State which parasite is depicted.
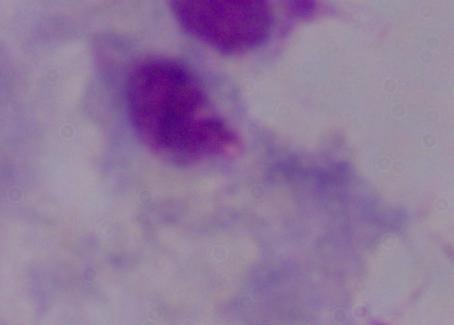

A trichomonad.

magnification = 1000x
modality = photomicrograph